Identify the parasite.
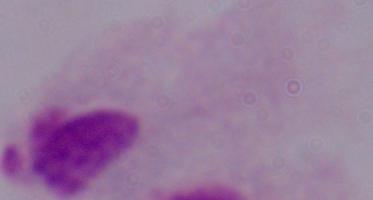

This is a trichomonad.

Micrograph. Captured at 1000x magnification.